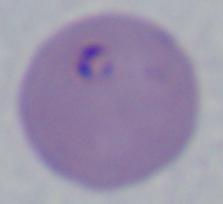
identification = Babesia
modality = micrograph
magnification = 1000x